Assess the morphology of the erythrocytes.
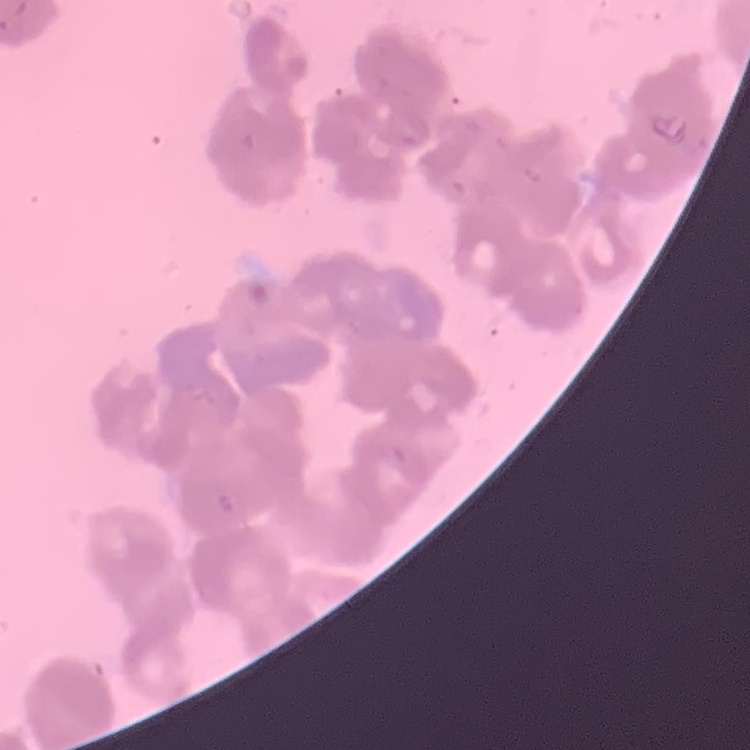

Rouleaux formation.

{
  "image_type": "square crop of a larger photomicrograph",
  "preparation": "thin blood film",
  "stain": "Field's or Giemsa"
}